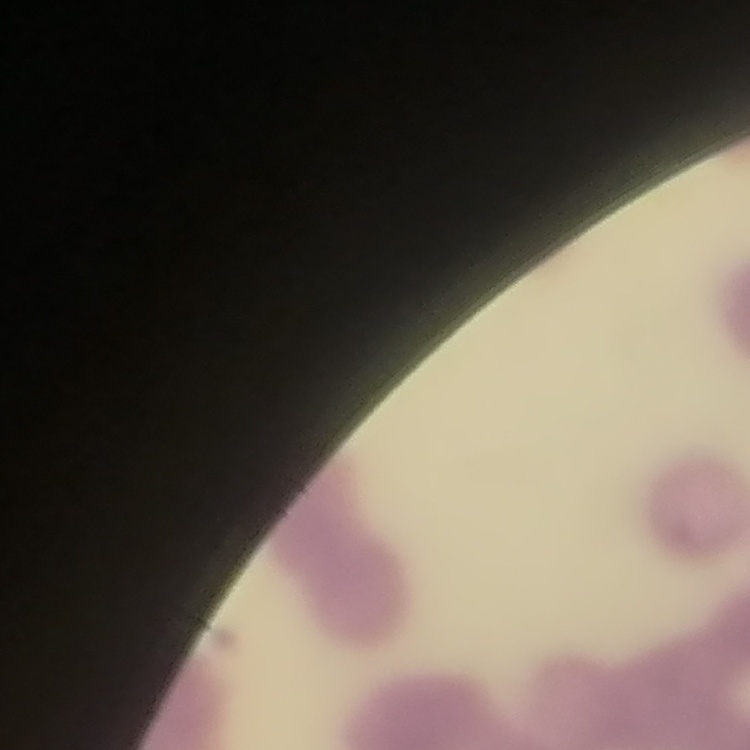
The erythrocytes exhibit rouleaux formation. Thin blood film. One tile cut from a larger photomicrograph. Field's or Giemsa stain.